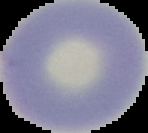
preparation = thin blood film
image type = segmented cell region on a black background
image size = 148×133 pixels
malaria status = uninfected